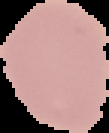

From a thin blood smear. Malaria status: uninfected. Image is 109×133 pixels. Segmented cell region on a black background.